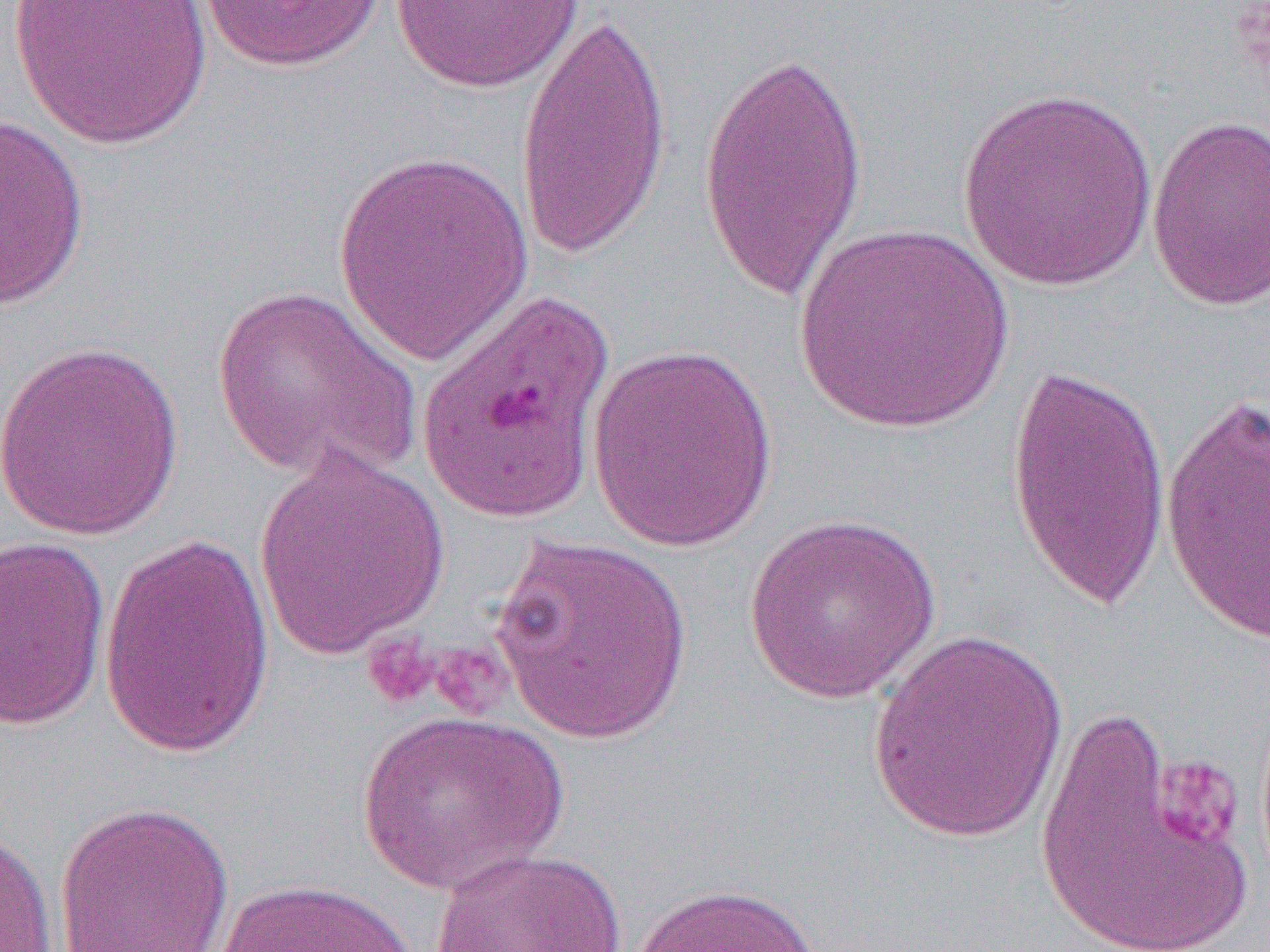 Approximate bounding boxes as (x1,y1)-(x2,y2) corner pairs in pixels. Uninfected red blood cell locations: (8,0)-(212,148), (198,0)-(385,73), (388,0)-(583,94), (514,5)-(672,267), (695,40)-(871,303), (955,86)-(1159,292), (0,113)-(90,310), (1146,115)-(1269,312), (331,147)-(536,368), (792,223)-(1015,434), (209,284)-(424,486), (0,338)-(185,541), (586,342)-(779,553), (1003,359)-(1170,617), (1159,388)-(1270,648), (252,443)-(452,662), (742,512)-(942,705), (487,531)-(695,746), (0,534)-(111,731), (96,534)-(276,760), (867,628)-(1070,845), (1033,702)-(1253,952), (355,711)-(570,894), (52,800)-(235,952), (0,824)-(58,951), (429,847)-(626,952), (212,877)-(420,952), (631,882)-(823,952). Platelet locations: (363,633)-(438,710), (425,640)-(513,719), (1152,754)-(1245,851). Slide-level diagnosis: Plasmodium falciparum. Image is 1270×952 pixels. Captured at 1000x magnification. Optical microscopy. Thin blood film. One field of a larger specimen.